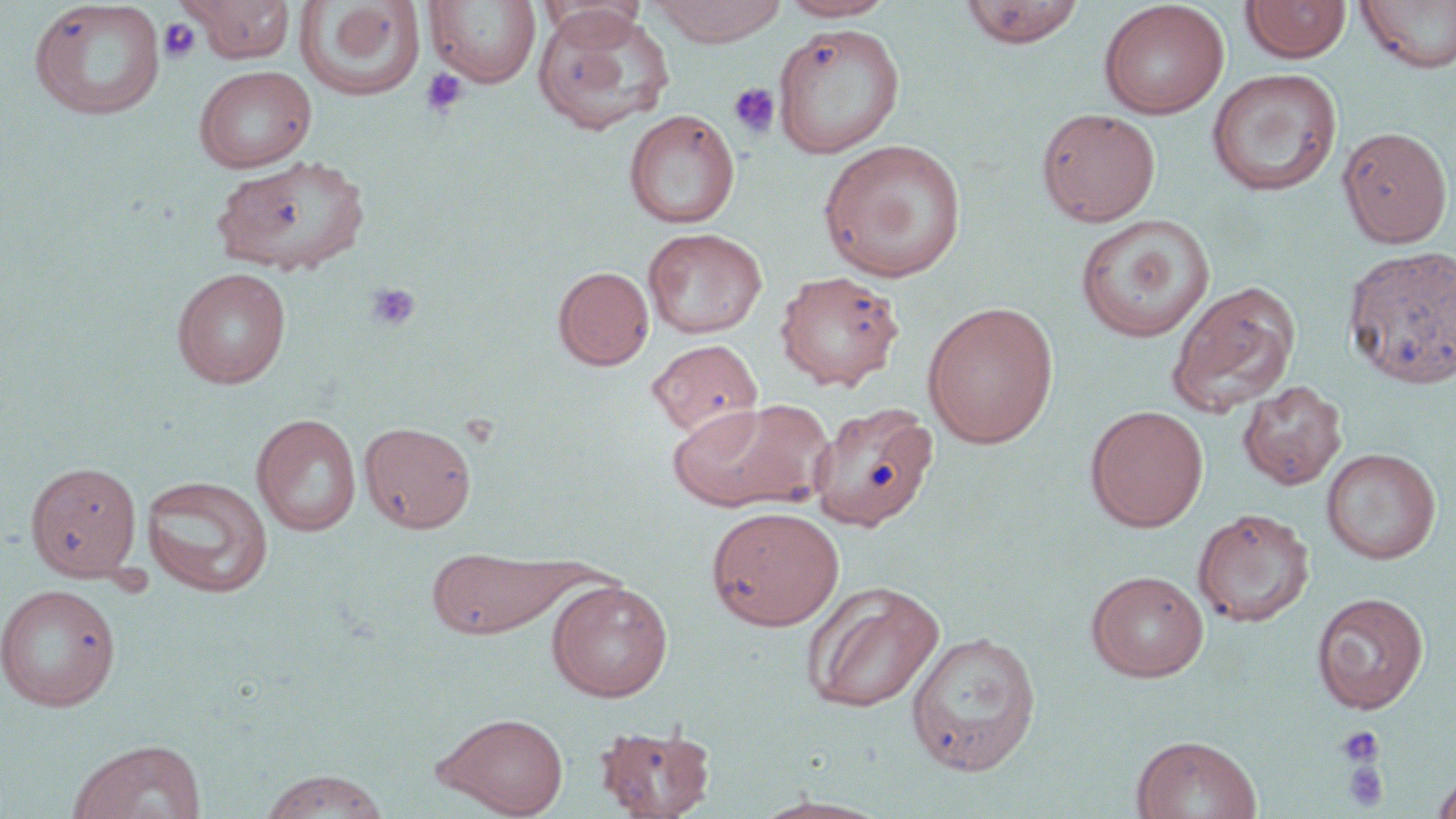

slide-level diagnosis = negative for blood parasites
uninfected red blood cell locations = approximate bounding boxes as [x1, y1, x2, y2] in pixels: [182, 0, 296, 64], [295, 0, 427, 101], [650, 0, 788, 46], [778, 0, 896, 21], [960, 0, 1084, 48], [1099, 0, 1229, 119], [1355, 0, 1456, 74], [28, 1, 167, 120], [423, 1, 542, 88], [538, 1, 646, 48], [1240, 1, 1351, 63], [533, 7, 674, 135], [773, 22, 905, 158], [193, 65, 317, 173], [1206, 67, 1343, 197], [1036, 107, 1161, 227], [623, 109, 740, 229], [1337, 125, 1454, 248], [819, 139, 967, 282], [212, 153, 370, 276], [1074, 213, 1215, 343], [642, 227, 767, 339], [1341, 245, 1456, 390], [552, 265, 654, 370], [171, 266, 292, 388], [774, 269, 905, 391], [1166, 280, 1301, 418], [922, 300, 1059, 449], [646, 338, 762, 439], [1237, 380, 1347, 491], [667, 397, 833, 514], [811, 401, 939, 531], [1084, 404, 1209, 531], [251, 413, 363, 537], [359, 421, 476, 533], [1321, 447, 1441, 564], [24, 461, 143, 582], [140, 474, 274, 598], [706, 505, 845, 631], [1192, 507, 1314, 627], [426, 545, 574, 640], [1085, 569, 1208, 682], [547, 579, 673, 701], [801, 580, 945, 712], [0, 583, 121, 711], [1311, 592, 1429, 714], [905, 630, 1041, 776], [435, 712, 569, 817], [594, 723, 715, 818], [1131, 734, 1262, 819], [67, 739, 208, 819], [1431, 768, 1456, 819], [256, 769, 392, 818], [753, 794, 890, 818]
image size = 1456×819 pixels
preparation = thin blood film
platelet locations = approximate bounding boxes as [x1, y1, x2, y2] in pixels: [158, 18, 201, 63], [419, 68, 469, 116], [728, 82, 780, 138], [366, 282, 420, 332], [1336, 726, 1384, 766], [1340, 760, 1391, 812]
field of view = one of a larger specimen
stain = May-Grünwald-Giemsa
modality = optical microscopy
magnification = 1000x